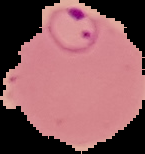
image size = 145×154 pixels
preparation = thin blood film
result = malaria parasites identified
image type = segmented cell region on a black background